Find each parasitized red blood cell.
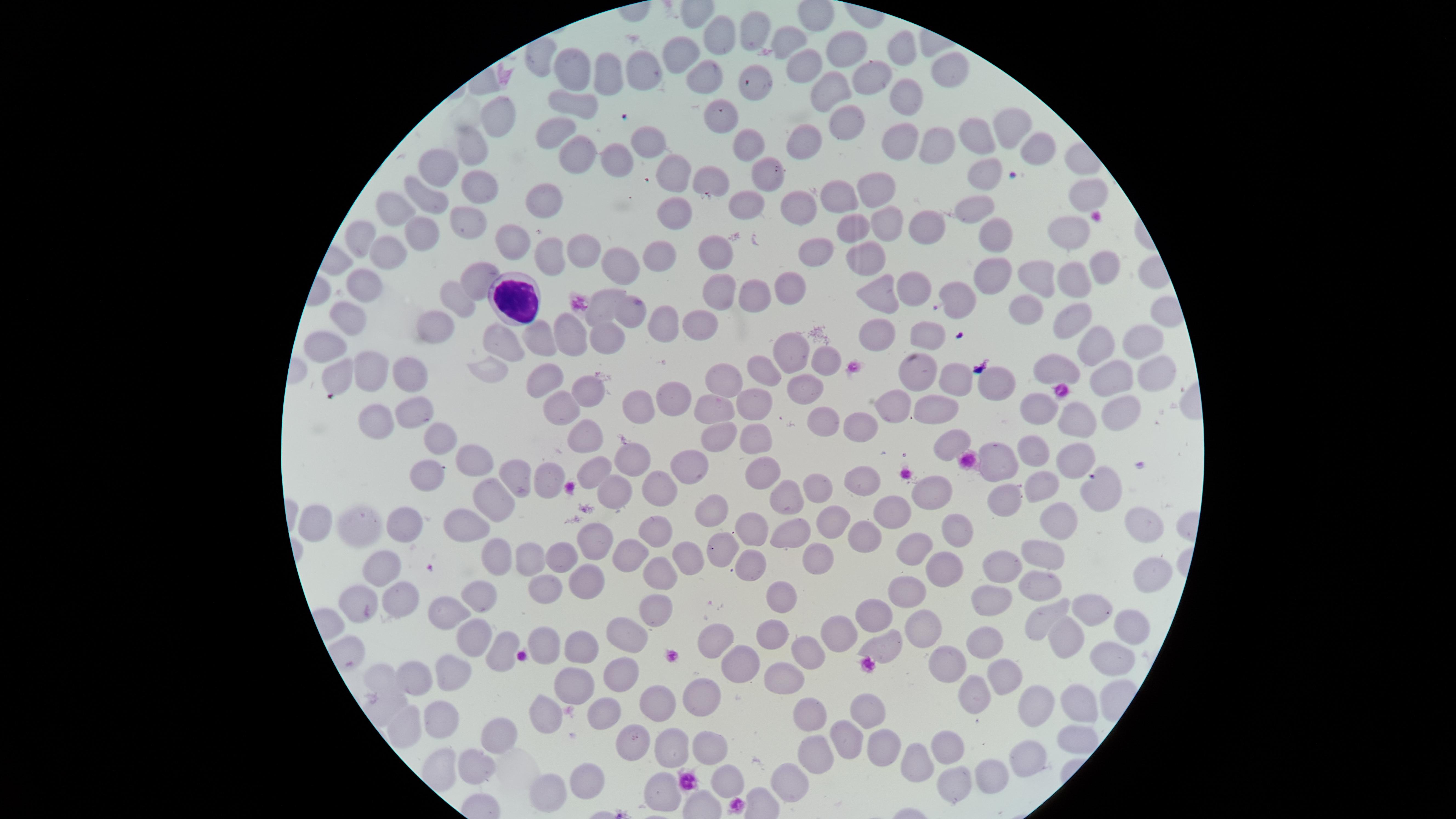

No parasitized red blood cells identified.

Approximate marker points as [x, y] in pixels. White blood cells: [516, 297]. Uninfected red blood cells: [752, 29], [720, 36], [791, 36], [843, 45], [678, 52], [904, 54], [798, 62], [943, 66], [574, 69], [604, 72], [638, 73], [705, 75], [873, 81], [759, 86], [829, 88], [899, 98], [567, 100], [728, 117], [496, 118], [1010, 122], [553, 126], [842, 128], [979, 135], [645, 138], [904, 138], [931, 144], [473, 146], [750, 146], [801, 148], [1032, 150], [573, 151], [617, 158], [440, 164], [671, 168], [985, 170], [713, 179], [767, 179], [476, 182], [875, 187], [544, 194], [848, 195], [421, 196], [1085, 198], [747, 206], [396, 207], [803, 207], [974, 210], [891, 215], [677, 217], [470, 223], [850, 224], [931, 227], [361, 235], [416, 236], [1064, 239], [516, 241], [1001, 242], [720, 245], [822, 245], [579, 248], [546, 252], [868, 252], [379, 255], [660, 257], [612, 260], [1100, 271], [990, 272], [1041, 276], [1070, 280], [359, 283], [481, 283], [785, 286], [916, 289], [876, 292], [755, 293], [720, 294], [955, 297], [456, 298], [1030, 306], [630, 309], [591, 313], [1071, 316], [347, 319], [662, 322], [432, 326], [701, 331], [567, 336], [599, 337], [934, 337], [873, 338], [1143, 339], [508, 340], [542, 341], [327, 344], [790, 349], [1093, 349], [820, 356], [487, 367], [365, 370], [1052, 370], [761, 372], [1149, 372], [331, 373], [545, 375], [724, 376], [914, 376], [952, 376], [404, 378], [1112, 379], [1006, 383], [803, 388], [590, 391], [674, 398], [937, 403], [707, 404], [749, 405], [554, 406], [635, 406], [1116, 408], [897, 409], [1038, 409], [408, 411], [368, 419], [1083, 419], [821, 423], [859, 424], [713, 432], [587, 434], [755, 434], [946, 441], [438, 442], [1034, 447], [630, 456], [996, 456], [1079, 458], [475, 459], [693, 464], [597, 469], [422, 475], [766, 475], [514, 476], [552, 480], [860, 481], [1038, 481], [660, 486], [815, 489], [1090, 489], [611, 492], [999, 492], [928, 493], [788, 497], [492, 501], [712, 507], [886, 517], [322, 519], [834, 521], [1054, 521], [358, 522], [404, 523], [959, 525], [468, 526], [1141, 526], [756, 529], [654, 531], [787, 532], [862, 539], [599, 545], [719, 545], [499, 550], [919, 551], [1053, 551], [534, 556], [564, 556], [689, 557], [630, 558], [816, 561], [377, 568], [1001, 568], [945, 569], [750, 570], [664, 576], [1146, 576], [580, 583], [1038, 585], [541, 588], [476, 596], [783, 596], [908, 596], [396, 599], [988, 599], [355, 605], [660, 607], [1096, 609], [450, 615], [876, 616], [1042, 619], [1126, 625], [632, 630], [920, 631], [473, 632], [769, 632], [827, 636], [719, 639], [1059, 641], [580, 642], [988, 642], [884, 647], [501, 652], [803, 654], [947, 656], [1107, 660], [739, 664], [623, 669], [423, 670], [455, 671], [781, 671], [1009, 671], [385, 677], [572, 683], [695, 693], [971, 693], [1081, 698], [662, 701], [868, 707], [1042, 709], [805, 710], [539, 714], [607, 715], [439, 716], [399, 733], [844, 734], [630, 737], [1064, 738], [883, 744], [492, 745], [673, 749], [945, 749], [710, 751], [1026, 754], [812, 756], [916, 759], [478, 766], [991, 773], [786, 775], [726, 779], [588, 781], [948, 784], [667, 786], [552, 793]. Smartphone photograph through the microscope eyepiece. Image is 1456×819 pixels. Giemsa-stained preparation. The visible region is circular. Thin blood film. Single field of view.